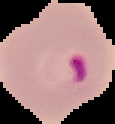 From a thin blood smear. Result: malaria parasites detected. The area outside the segmented cell region is set to black. Image is 115×124 pixels.